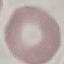 Malaria status: uninfected. Automatically extracted cell patch, resized to 64 × 64 pixels. Photographed with a smartphone camera at the microscope eyepiece. Thin blood smear. Giemsa stain.